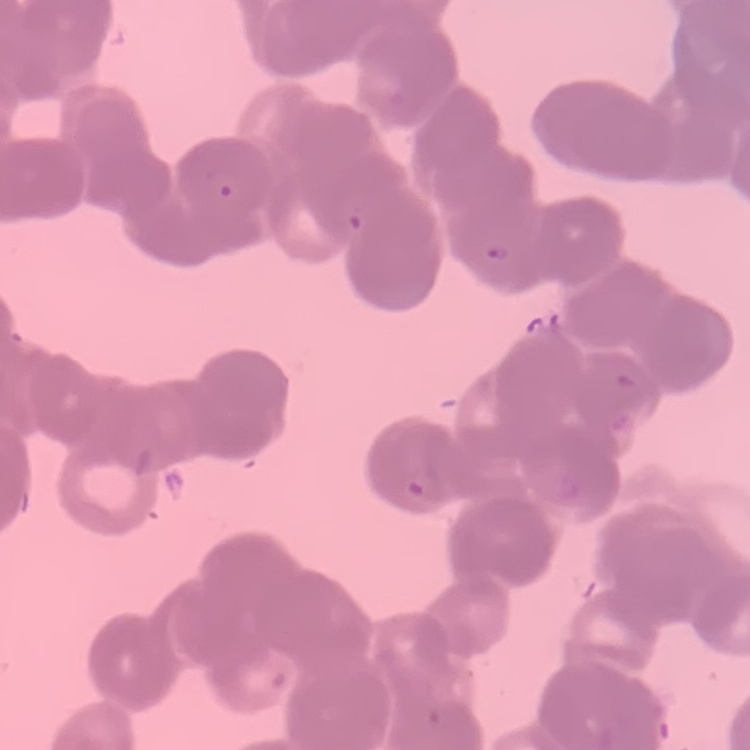

Summary:
  - Red blood cell morphology: rouleaux formation
  - Preparation: thin peripheral smear
  - Image type: square crop of a larger photomicrograph
  - Stain: Field's or Giemsa